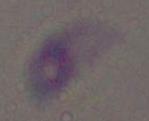

Micrograph. Captured at 1000x magnification. Toxoplasma gondii is seen.